State which cell type is depicted.
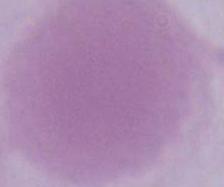

This is an erythrocyte.

Photomicrograph. Captured at 1000x magnification.